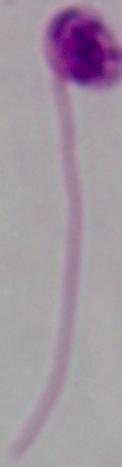 1000x magnification. A Leishmania parasite is shown. Micrograph.